Report the malaria status of this cell.
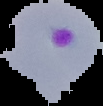

Parasitized.

image_size: 103×106 pixels
image_type: cell region segmented out of the field of view; surrounding area masked to black
preparation: thin blood smear